Describe the morphology of the red blood cells.
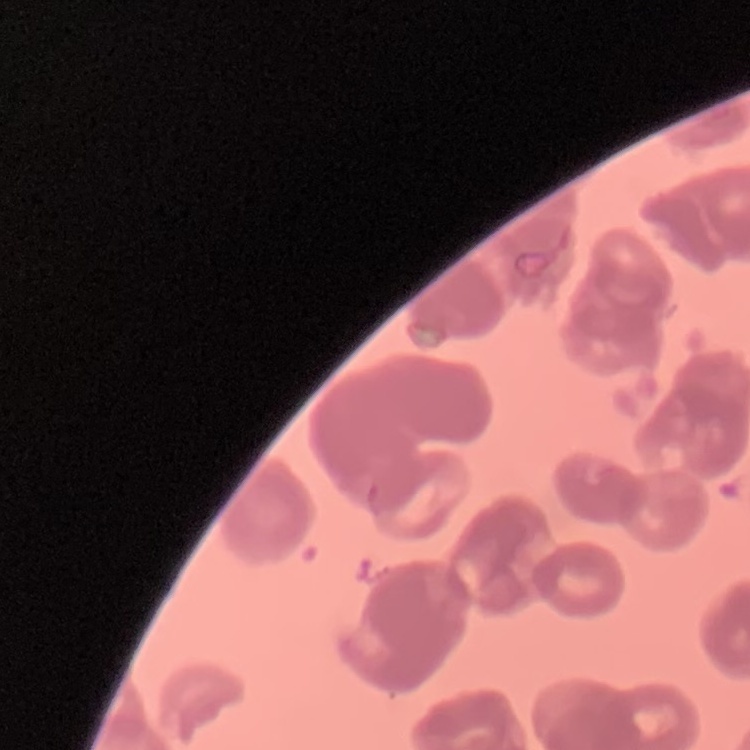
They show rouleaux formation.

One tile cut from a larger photomicrograph. Thin blood smear. Stained with either Field's or Giemsa.